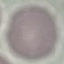

Summary:
  - Malaria status: uninfected
  - Preparation: thin blood smear
  - Image type: automatically extracted cell patch, resized to 64 × 64 pixels
  - Stain: Giemsa
  - Capture: smartphone camera at the microscope eyepiece